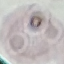

Summary:
  - Result: no malaria parasites seen
  - Preparation: thin blood film
  - Image type: automatically extracted cell patch, resized to 64 × 64 pixels
  - Capture: smartphone camera at the microscope eyepiece
  - Stain: Giemsa